Comment on the morphology of the erythrocytes.
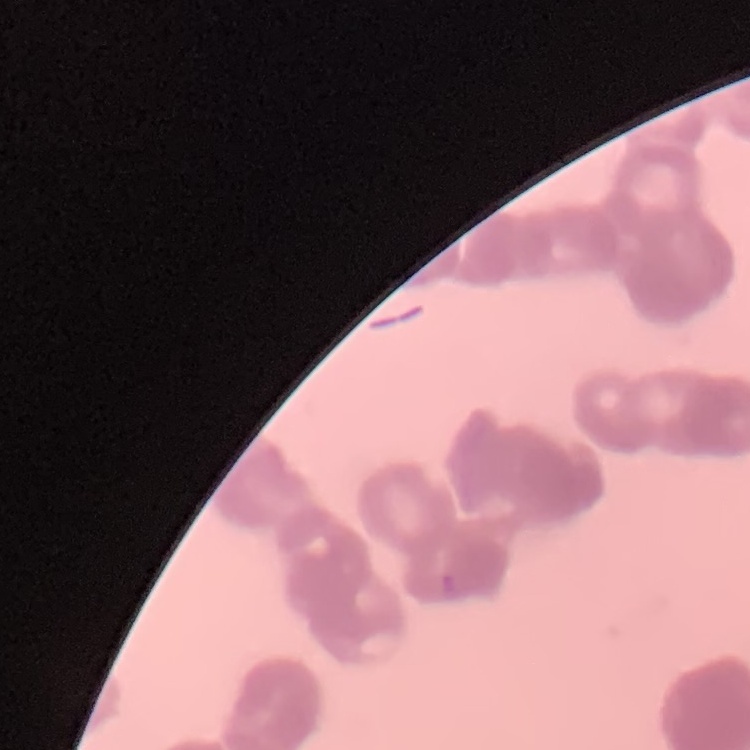

They show rouleaux formation.

Thin blood film. Stained with either Field's or Giemsa. One tile cut from a larger photomicrograph.